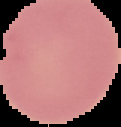 Result: no malaria parasites seen. The area outside the segmented cell region is set to black. From a thin blood smear. Image is 121×127 pixels.